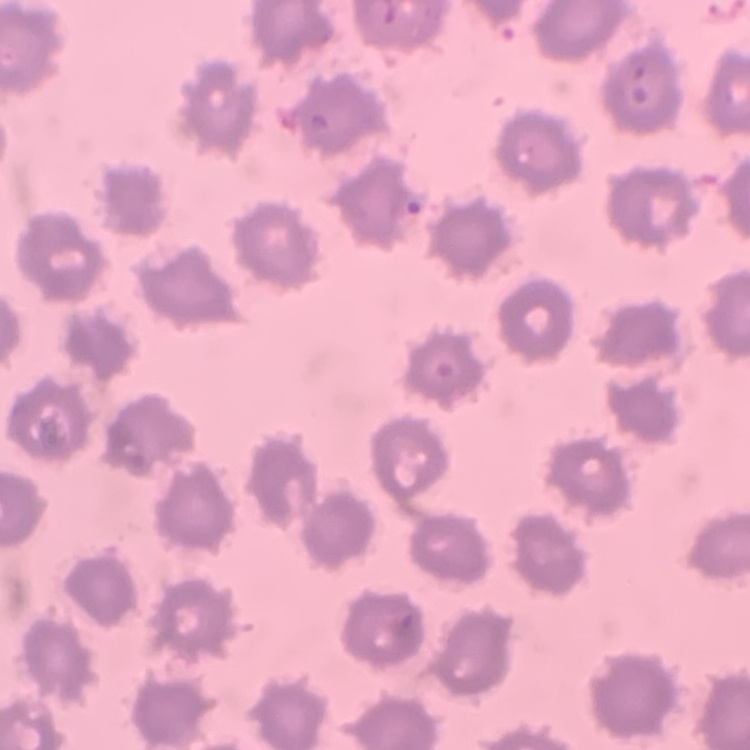

erythrocyte_morphology: no rouleaux formation
image_type: one tile cut from a larger photomicrograph
stain: Field's or Giemsa
preparation: thin blood smear